Give the position of every Plasmodium parasite.
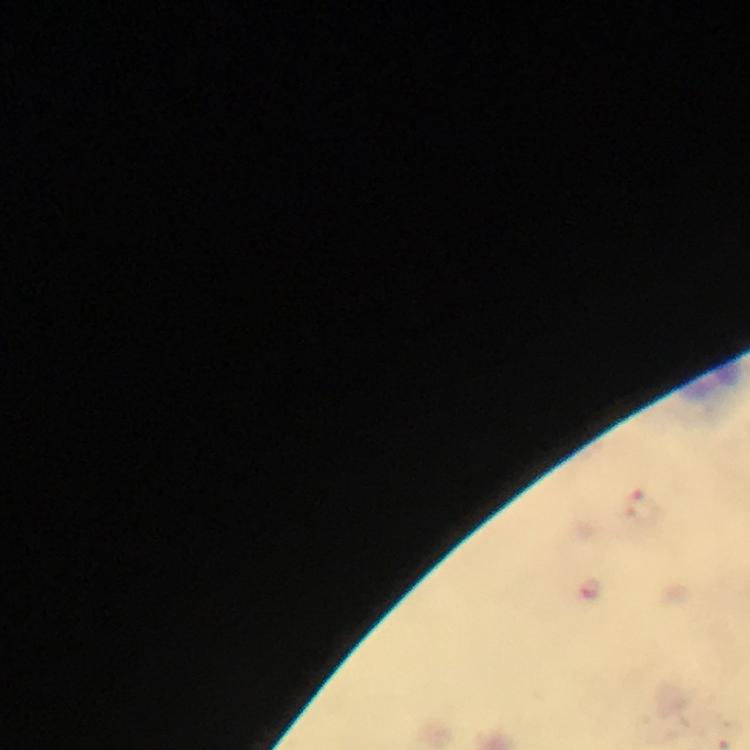

Approximate centers as [x, y] in pixels.
Plasmodium parasites: [643, 507], [592, 589].

immersion_oil: applied
cropped_from: one field of view
capture: smartphone camera through the microscope
preparation: thick blood smear
stain: Giemsa
image_size: 750×750 pixels
magnification: 100x
context: from a malaria diagnostic workup